Describe the morphology of the erythrocytes.
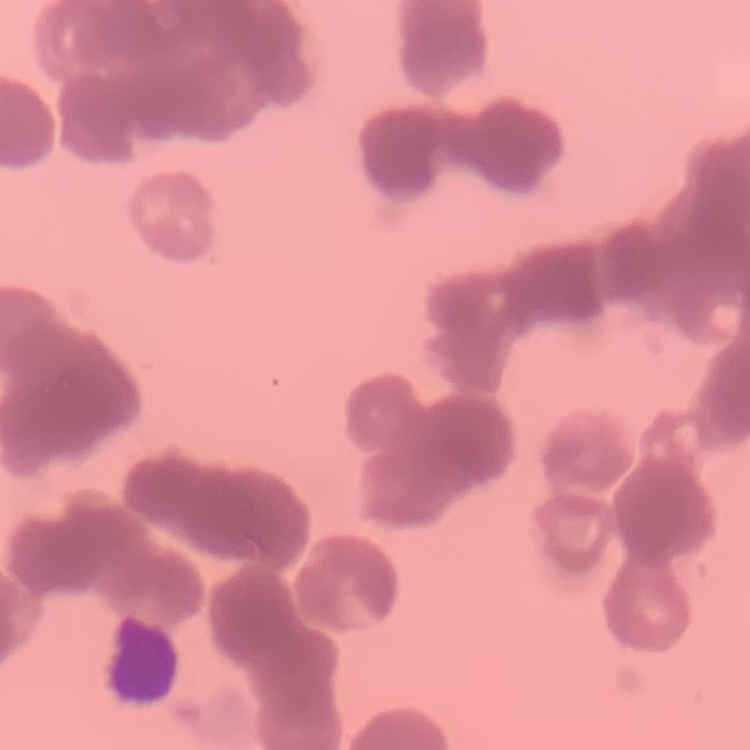

They show rouleaux formation.

Summary:
  - Preparation: thin blood film
  - Image type: one tile cut from a larger photomicrograph
  - Stain: Field's or Giemsa